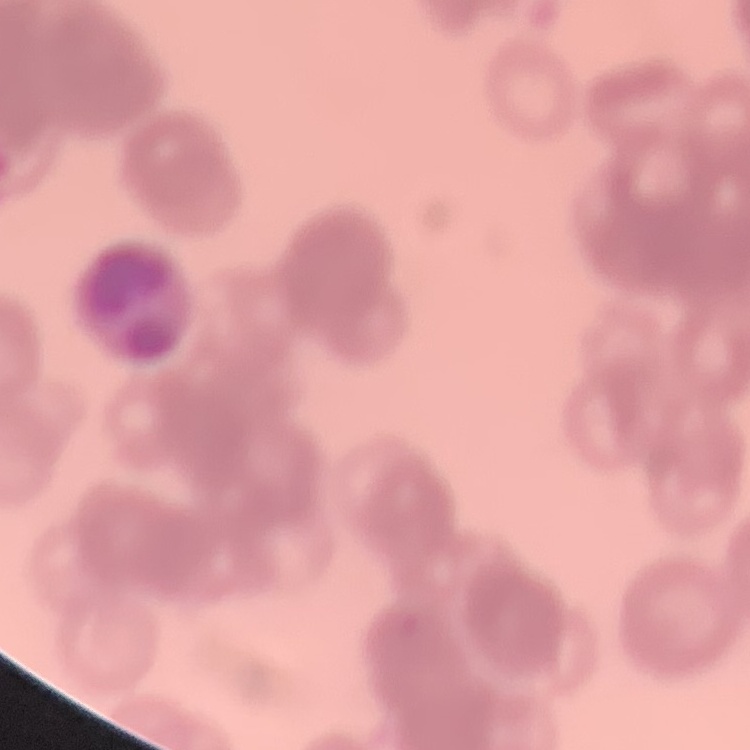

The erythrocytes exhibit rouleaux formation. Thin peripheral smear. Square crop of a larger photomicrograph. Field's or Giemsa stain.